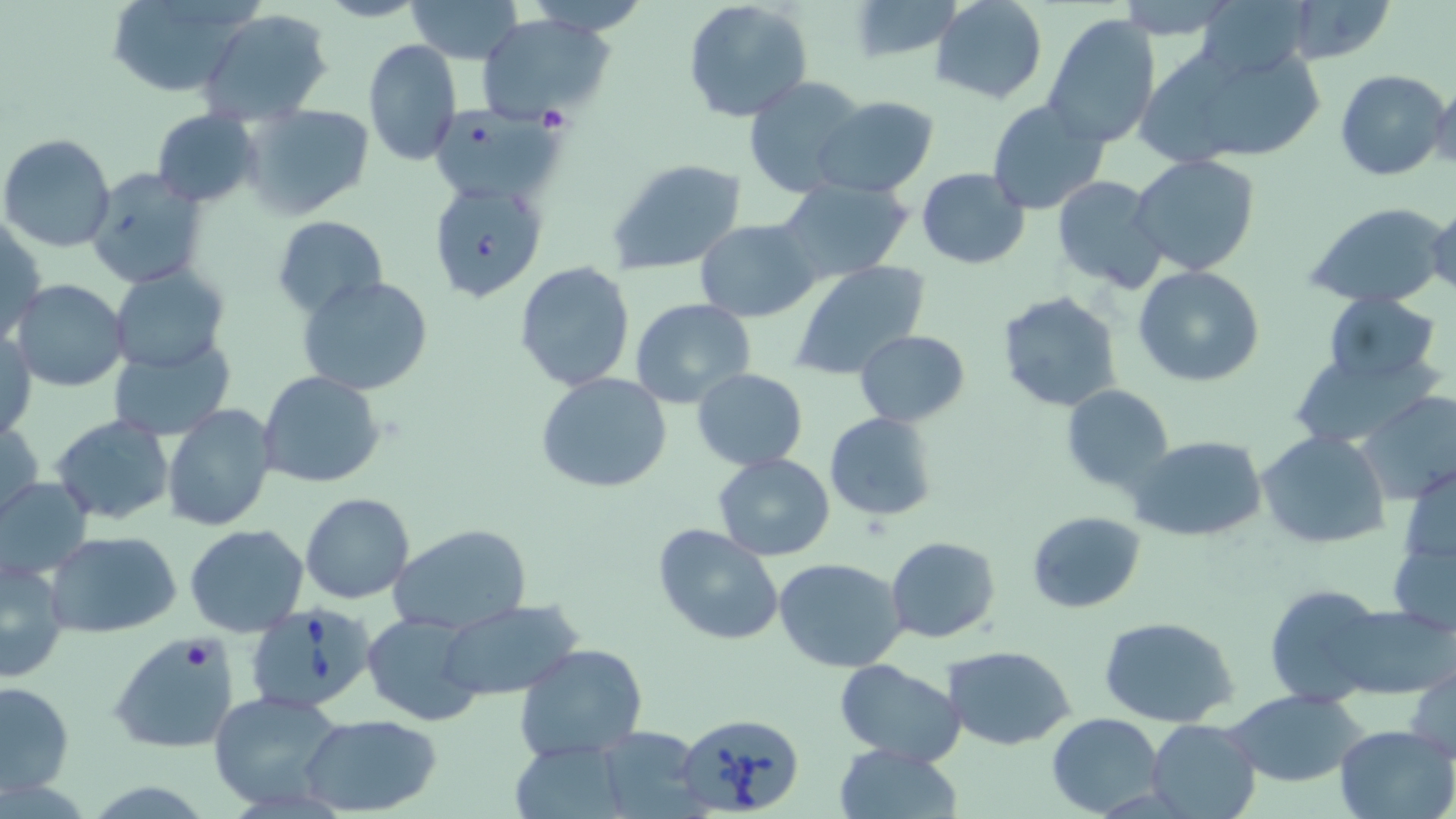
Summary:
  - Coordinate format: approximate bounding boxes as named x1/y1/x2/y2 corners in pixels
  - Uninfected red blood cell locations: (x1=102, y1=0, x2=260, y2=97), (x1=317, y1=0, x2=425, y2=23), (x1=405, y1=0, x2=524, y2=65), (x1=682, y1=0, x2=814, y2=124), (x1=932, y1=0, x2=1048, y2=105), (x1=1115, y1=0, x2=1242, y2=37), (x1=1195, y1=0, x2=1314, y2=80), (x1=1278, y1=0, x2=1396, y2=66), (x1=526, y1=1, x2=653, y2=36), (x1=849, y1=1, x2=963, y2=62), (x1=199, y1=7, x2=331, y2=124), (x1=1042, y1=13, x2=1161, y2=150), (x1=476, y1=15, x2=612, y2=124), (x1=363, y1=40, x2=462, y2=168), (x1=1146, y1=45, x2=1328, y2=166), (x1=1335, y1=68, x2=1448, y2=182), (x1=1430, y1=75, x2=1456, y2=175), (x1=744, y1=76, x2=871, y2=196), (x1=812, y1=96, x2=940, y2=198), (x1=988, y1=100, x2=1111, y2=217), (x1=240, y1=103, x2=375, y2=220), (x1=151, y1=109, x2=261, y2=207), (x1=429, y1=110, x2=565, y2=206), (x1=1, y1=133, x2=116, y2=253), (x1=1130, y1=154, x2=1261, y2=277), (x1=608, y1=161, x2=751, y2=277), (x1=84, y1=163, x2=211, y2=291), (x1=915, y1=167, x2=1030, y2=269), (x1=1051, y1=175, x2=1169, y2=294), (x1=774, y1=178, x2=914, y2=284), (x1=428, y1=183, x2=546, y2=298), (x1=1427, y1=200, x2=1455, y2=299), (x1=1305, y1=202, x2=1448, y2=309), (x1=272, y1=215, x2=387, y2=319), (x1=1, y1=218, x2=46, y2=346), (x1=695, y1=218, x2=820, y2=322), (x1=514, y1=260, x2=636, y2=392), (x1=792, y1=260, x2=932, y2=383), (x1=110, y1=265, x2=230, y2=374), (x1=1133, y1=266, x2=1265, y2=387), (x1=296, y1=274, x2=434, y2=396), (x1=11, y1=278, x2=129, y2=391), (x1=996, y1=290, x2=1122, y2=413), (x1=1321, y1=293, x2=1441, y2=386), (x1=629, y1=297, x2=756, y2=408), (x1=1, y1=328, x2=36, y2=444), (x1=854, y1=329, x2=972, y2=426), (x1=106, y1=337, x2=236, y2=439), (x1=1289, y1=354, x2=1432, y2=446), (x1=691, y1=367, x2=809, y2=471), (x1=258, y1=371, x2=386, y2=490), (x1=535, y1=373, x2=675, y2=494), (x1=1060, y1=382, x2=1174, y2=493), (x1=1358, y1=391, x2=1456, y2=506), (x1=163, y1=404, x2=276, y2=532), (x1=824, y1=412, x2=940, y2=523), (x1=51, y1=415, x2=176, y2=526), (x1=0, y1=417, x2=44, y2=524), (x1=1256, y1=430, x2=1391, y2=551), (x1=1128, y1=435, x2=1268, y2=542), (x1=713, y1=453, x2=835, y2=561), (x1=1401, y1=464, x2=1456, y2=571), (x1=1, y1=476, x2=94, y2=582), (x1=300, y1=492, x2=414, y2=604), (x1=1026, y1=510, x2=1146, y2=613), (x1=651, y1=523, x2=784, y2=647), (x1=184, y1=524, x2=308, y2=637), (x1=390, y1=524, x2=532, y2=633), (x1=43, y1=531, x2=183, y2=639), (x1=1387, y1=531, x2=1456, y2=637), (x1=885, y1=536, x2=999, y2=642), (x1=1, y1=553, x2=72, y2=682), (x1=774, y1=557, x2=908, y2=673), (x1=1262, y1=586, x2=1389, y2=706), (x1=434, y1=601, x2=583, y2=703), (x1=1332, y1=603, x2=1452, y2=700), (x1=362, y1=612, x2=484, y2=726), (x1=1099, y1=616, x2=1241, y2=728), (x1=109, y1=632, x2=240, y2=755), (x1=514, y1=643, x2=647, y2=763), (x1=944, y1=646, x2=1075, y2=749), (x1=833, y1=660, x2=967, y2=767), (x1=1407, y1=660, x2=1456, y2=764), (x1=1, y1=680, x2=74, y2=799), (x1=1226, y1=690, x2=1365, y2=787), (x1=207, y1=693, x2=344, y2=811), (x1=1046, y1=712, x2=1164, y2=818), (x1=300, y1=714, x2=444, y2=816), (x1=1147, y1=718, x2=1261, y2=819), (x1=1334, y1=723, x2=1455, y2=819), (x1=592, y1=727, x2=705, y2=816), (x1=834, y1=744, x2=961, y2=819)
  - Babesia divergens-infected red blood cell locations: (x1=246, y1=604, x2=377, y2=716), (x1=676, y1=711, x2=805, y2=817)
  - Slide-level diagnosis: Babesia divergens
  - Preparation: thin blood smear
  - Modality: optical microscopy
  - Field of view: one of a larger specimen
  - Image size: 1456×819 pixels
  - Stain: May-Grünwald-Giemsa
  - Magnification: 1000x